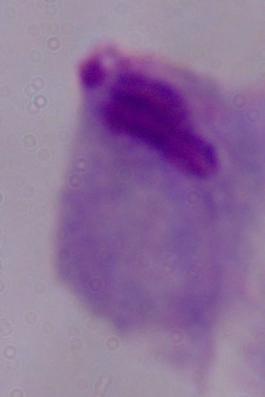

A trichomonad is shown. 1000x magnification. Micrograph.